Point out each malaria parasite and classify it by life-cycle stage.
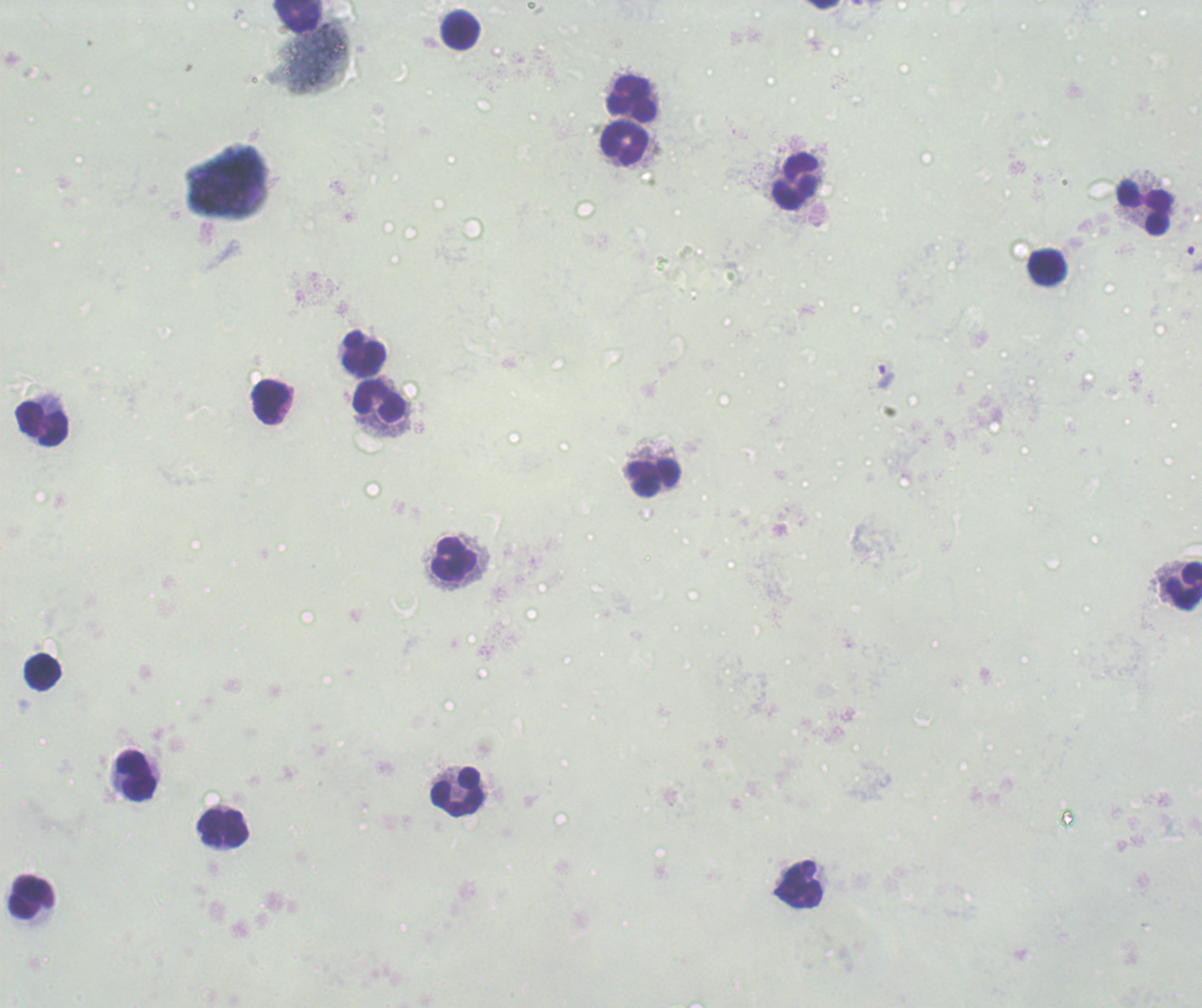

Approximate centers as (x, y) in pixels.
Trophozoites: (1194, 259), (886, 376).
No schizont or gametocyte forms observed.

Approximate centers as (x, y) in pixels.
Summary:
  - Leukocyte locations: (824, 6), (294, 16), (461, 29), (632, 99), (624, 143), (796, 181), (1143, 207), (1047, 267), (364, 356), (379, 400), (270, 402), (43, 424), (652, 478), (455, 560), (1182, 585), (43, 673), (133, 776), (458, 792), (224, 830), (801, 882), (31, 898)
  - Context: previously used in an actual diagnosis
  - Image size: 1202×1008 pixels
  - Background quality: unsatisfactory
  - Preparation: thick smear of blood
  - Magnification: 100x
  - Stain: Romanowsky
  - Field of view: single